Report the malaria status of this cell.
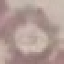
It is uninfected.

stain = Giemsa
capture = smartphone through the microscope eyepiece
preparation = thin smear
image type = cell patch, automatically extracted from a larger field of view and resized to 64 × 64 pixels